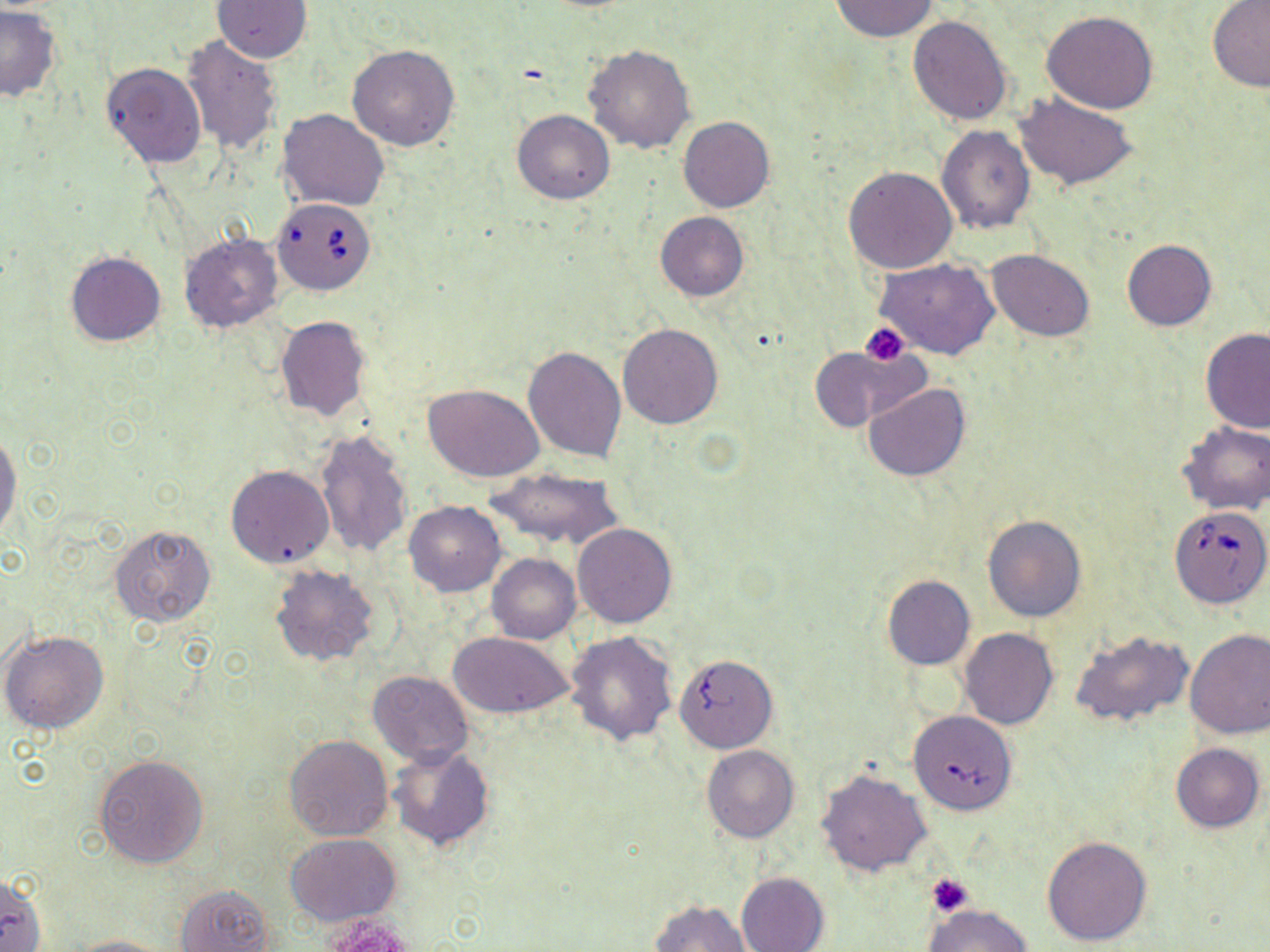

Approximate bounding boxes as [x1, y1, x2, y2] in pixels. Babesia divergens-infected red blood cell locations: [271, 198, 376, 296], [1170, 516, 1267, 608]. Platelet locations: [860, 323, 911, 366], [926, 872, 975, 916]. Uninfected red blood cell locations: [212, 0, 312, 63], [832, 0, 938, 41], [1207, 1, 1270, 91], [0, 6, 61, 101], [1042, 10, 1158, 114], [908, 14, 1013, 125], [180, 35, 284, 157], [347, 45, 460, 152], [583, 45, 695, 155], [101, 62, 206, 169], [1015, 93, 1137, 191], [277, 108, 390, 211], [512, 109, 614, 204], [678, 116, 775, 212], [937, 125, 1036, 234], [844, 165, 957, 274], [654, 212, 748, 301], [180, 232, 284, 331], [1122, 239, 1217, 331], [987, 249, 1095, 341], [64, 251, 166, 346], [875, 258, 999, 361], [275, 316, 370, 422], [617, 324, 724, 429], [1201, 329, 1270, 434], [523, 345, 627, 461], [809, 345, 929, 434], [422, 383, 547, 484], [864, 384, 970, 482], [1176, 421, 1270, 515], [315, 429, 413, 559], [0, 431, 21, 544], [225, 465, 335, 569], [487, 467, 625, 549], [403, 500, 505, 597], [983, 516, 1087, 622], [573, 523, 676, 628], [109, 524, 219, 629], [487, 554, 580, 644], [269, 563, 381, 667], [882, 576, 975, 670], [959, 628, 1058, 730], [1184, 628, 1270, 739], [2, 629, 109, 733], [1070, 630, 1193, 729], [448, 631, 577, 720], [567, 632, 679, 747], [676, 655, 775, 752], [367, 671, 474, 765], [909, 716, 1017, 814], [283, 734, 394, 841], [1170, 743, 1265, 832], [702, 744, 799, 843], [388, 746, 493, 851], [94, 755, 209, 868], [815, 768, 932, 877], [285, 833, 401, 925], [1042, 836, 1153, 947], [736, 872, 829, 952], [0, 874, 45, 952], [175, 884, 274, 952], [649, 899, 751, 951], [925, 905, 1031, 952], [314, 914, 420, 952], [67, 935, 175, 952]. Slide-level diagnosis: Babesia divergens. May-Grünwald-Giemsa stain. One field of a larger specimen. Thin blood film. Captured at 1000x magnification. Light microscopy. Image is 1270×952 pixels.